Locate and identify every blood parasite.
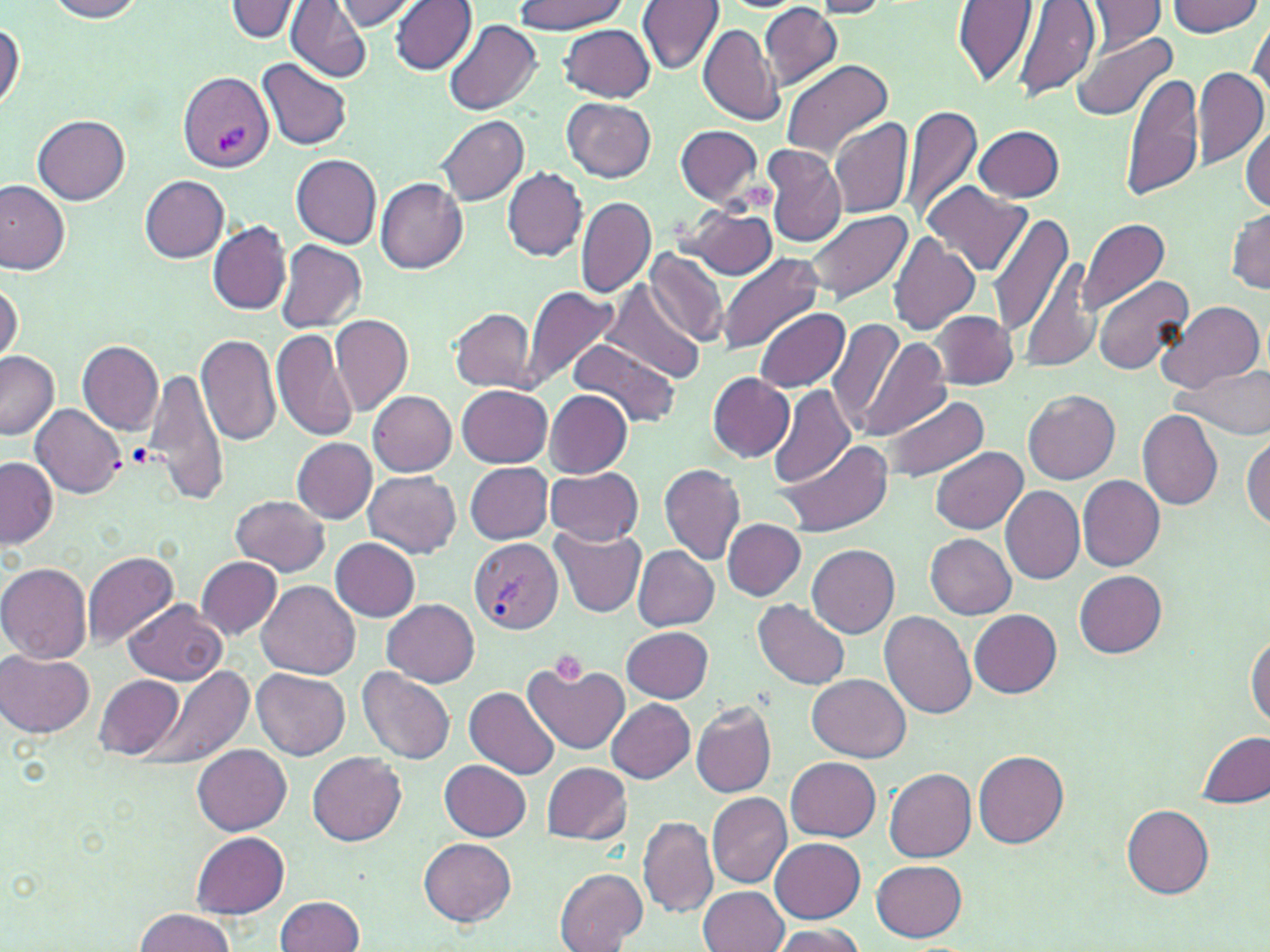
Approximate bounding boxes as named x1/y1/x2/y2 corners in pixels.
Plasmodium vivax-infected red blood cells: (x1=177, y1=70, x2=274, y2=175), (x1=470, y1=538, x2=563, y2=634).
No Plasmodium falciparum, Plasmodium ovale, Plasmodium malariae, Babesia divergens, or Trypanosoma brucei observed.

Summary:
  - Platelet locations: (x1=127, y1=442, x2=155, y2=468), (x1=550, y1=648, x2=588, y2=683)
  - Uninfected red blood cell locations: (x1=44, y1=0, x2=145, y2=22), (x1=224, y1=0, x2=303, y2=42), (x1=286, y1=0, x2=369, y2=83), (x1=336, y1=0, x2=420, y2=29), (x1=515, y1=0, x2=625, y2=34), (x1=636, y1=0, x2=724, y2=75), (x1=953, y1=0, x2=1038, y2=89), (x1=1167, y1=0, x2=1263, y2=37), (x1=391, y1=1, x2=477, y2=74), (x1=807, y1=1, x2=892, y2=18), (x1=1013, y1=1, x2=1101, y2=102), (x1=1083, y1=1, x2=1164, y2=50), (x1=760, y1=4, x2=844, y2=90), (x1=1247, y1=16, x2=1269, y2=101), (x1=0, y1=19, x2=25, y2=113), (x1=444, y1=21, x2=542, y2=115), (x1=560, y1=22, x2=656, y2=101), (x1=698, y1=23, x2=780, y2=125), (x1=1071, y1=31, x2=1177, y2=122), (x1=257, y1=58, x2=354, y2=151), (x1=779, y1=59, x2=892, y2=160), (x1=1192, y1=67, x2=1269, y2=170), (x1=1121, y1=70, x2=1203, y2=203), (x1=562, y1=97, x2=655, y2=182), (x1=903, y1=105, x2=981, y2=220), (x1=33, y1=115, x2=131, y2=204), (x1=437, y1=115, x2=529, y2=206), (x1=829, y1=117, x2=911, y2=218), (x1=675, y1=124, x2=765, y2=207), (x1=975, y1=124, x2=1067, y2=203), (x1=1241, y1=125, x2=1270, y2=214), (x1=791, y1=129, x2=893, y2=273), (x1=762, y1=146, x2=847, y2=247), (x1=292, y1=155, x2=382, y2=247), (x1=502, y1=167, x2=589, y2=261), (x1=140, y1=175, x2=229, y2=262), (x1=375, y1=178, x2=468, y2=275), (x1=0, y1=180, x2=71, y2=275), (x1=924, y1=182, x2=1031, y2=276), (x1=575, y1=196, x2=656, y2=298), (x1=681, y1=204, x2=779, y2=280), (x1=1228, y1=206, x2=1270, y2=293), (x1=802, y1=209, x2=913, y2=303), (x1=988, y1=212, x2=1074, y2=337), (x1=1077, y1=217, x2=1170, y2=314), (x1=208, y1=221, x2=291, y2=315), (x1=887, y1=233, x2=980, y2=337), (x1=274, y1=241, x2=367, y2=332), (x1=644, y1=248, x2=728, y2=346), (x1=717, y1=253, x2=824, y2=360), (x1=1021, y1=257, x2=1100, y2=372), (x1=1093, y1=276, x2=1194, y2=376), (x1=0, y1=278, x2=22, y2=367), (x1=602, y1=280, x2=706, y2=382), (x1=519, y1=284, x2=622, y2=392), (x1=1158, y1=300, x2=1265, y2=393), (x1=450, y1=308, x2=536, y2=391), (x1=753, y1=308, x2=850, y2=393), (x1=930, y1=312, x2=1018, y2=389), (x1=329, y1=314, x2=414, y2=416), (x1=827, y1=318, x2=904, y2=431), (x1=271, y1=327, x2=360, y2=443), (x1=197, y1=331, x2=280, y2=446), (x1=859, y1=338, x2=950, y2=439), (x1=568, y1=339, x2=679, y2=428), (x1=78, y1=340, x2=165, y2=436), (x1=0, y1=351, x2=59, y2=439), (x1=1179, y1=363, x2=1270, y2=440), (x1=142, y1=366, x2=229, y2=506), (x1=707, y1=372, x2=795, y2=461), (x1=456, y1=384, x2=552, y2=466), (x1=769, y1=384, x2=856, y2=486), (x1=367, y1=389, x2=457, y2=475), (x1=544, y1=389, x2=632, y2=477), (x1=1024, y1=389, x2=1121, y2=484), (x1=879, y1=393, x2=990, y2=482), (x1=31, y1=403, x2=125, y2=498), (x1=1136, y1=409, x2=1224, y2=511), (x1=1244, y1=436, x2=1270, y2=532), (x1=775, y1=437, x2=890, y2=536), (x1=292, y1=439, x2=376, y2=523), (x1=930, y1=446, x2=1026, y2=533), (x1=936, y1=451, x2=1045, y2=616), (x1=1, y1=457, x2=58, y2=547), (x1=465, y1=462, x2=553, y2=544), (x1=659, y1=463, x2=746, y2=564), (x1=545, y1=468, x2=643, y2=545), (x1=364, y1=472, x2=462, y2=558), (x1=1077, y1=474, x2=1165, y2=570), (x1=1001, y1=486, x2=1085, y2=584), (x1=230, y1=495, x2=329, y2=575), (x1=723, y1=519, x2=806, y2=600), (x1=551, y1=527, x2=646, y2=617), (x1=926, y1=533, x2=1016, y2=619), (x1=331, y1=538, x2=421, y2=621), (x1=807, y1=543, x2=900, y2=639), (x1=632, y1=545, x2=719, y2=631), (x1=82, y1=552, x2=178, y2=652), (x1=197, y1=557, x2=282, y2=638), (x1=0, y1=562, x2=91, y2=664), (x1=1074, y1=570, x2=1168, y2=658), (x1=257, y1=581, x2=360, y2=679), (x1=753, y1=598, x2=851, y2=690), (x1=381, y1=599, x2=480, y2=686), (x1=125, y1=600, x2=228, y2=684), (x1=879, y1=609, x2=977, y2=719), (x1=970, y1=610, x2=1062, y2=698), (x1=622, y1=625, x2=713, y2=704), (x1=1245, y1=631, x2=1270, y2=730), (x1=2, y1=650, x2=96, y2=738), (x1=522, y1=660, x2=631, y2=755), (x1=130, y1=667, x2=253, y2=771), (x1=358, y1=667, x2=454, y2=768), (x1=252, y1=669, x2=350, y2=760), (x1=809, y1=673, x2=911, y2=763), (x1=96, y1=675, x2=182, y2=758), (x1=464, y1=686, x2=561, y2=779), (x1=606, y1=698, x2=695, y2=783), (x1=691, y1=701, x2=777, y2=797), (x1=1197, y1=731, x2=1270, y2=809), (x1=193, y1=744, x2=291, y2=835), (x1=973, y1=750, x2=1069, y2=849), (x1=308, y1=752, x2=406, y2=846), (x1=786, y1=757, x2=880, y2=841), (x1=440, y1=759, x2=530, y2=840), (x1=541, y1=762, x2=632, y2=844), (x1=883, y1=767, x2=977, y2=863), (x1=707, y1=791, x2=792, y2=886), (x1=1122, y1=804, x2=1214, y2=899), (x1=638, y1=815, x2=718, y2=918), (x1=192, y1=832, x2=288, y2=918), (x1=771, y1=837, x2=865, y2=922), (x1=420, y1=838, x2=516, y2=926), (x1=871, y1=860, x2=966, y2=942), (x1=554, y1=867, x2=646, y2=950), (x1=697, y1=884, x2=787, y2=952), (x1=274, y1=895, x2=366, y2=951), (x1=134, y1=908, x2=235, y2=951), (x1=766, y1=923, x2=865, y2=952)
  - Slide-level diagnosis: Plasmodium vivax
  - Modality: light microscopy
  - Image size: 1270×952 pixels
  - Magnification: 1000x
  - Field of view: single
  - Preparation: thin blood smear
  - Stain: May-Grünwald-Giemsa